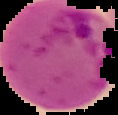
image size = 118×115 pixels
image type = cell region segmented out of the field of view; surrounding area masked to black
malaria status = parasitized
preparation = thin blood film